State the blood parasite species.
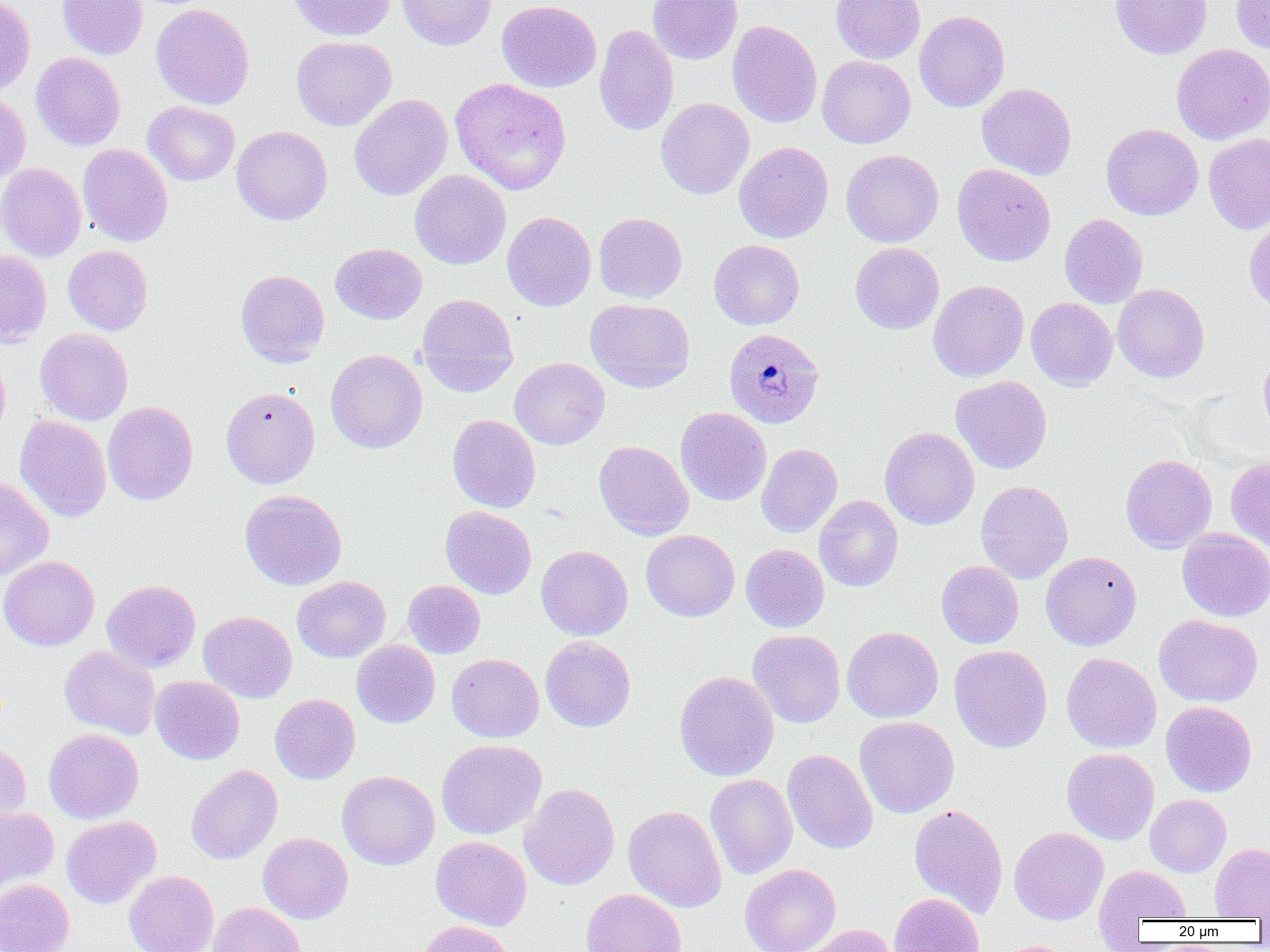
Plasmodium malariae.

image size = 1270×952 pixels
Plasmodium malariae-infected red blood cell locations = approximate bounding boxes as (x1,y1)-(x2,y2) corner pairs in pixels: (723,328)-(824,428)
uninfected red blood cell locations = approximate bounding boxes as (x1,y1)-(x2,y2) corner pairs in pixels: (0,0)-(35,98), (57,0)-(148,60), (287,0)-(395,41), (396,0)-(497,50), (497,0)-(601,92), (648,0)-(743,64), (831,0)-(925,63), (1110,0)-(1213,59), (1231,0)-(1270,54), (151,3)-(254,109), (914,11)-(1010,112), (727,20)-(822,128), (594,24)-(679,136), (291,36)-(397,131), (1171,44)-(1270,144), (30,52)-(125,151), (817,56)-(915,148), (450,77)-(571,195), (976,83)-(1077,180), (0,93)-(31,183), (349,94)-(453,201), (656,98)-(755,199), (143,101)-(240,186), (1101,124)-(1203,220), (231,126)-(332,225), (1203,132)-(1270,234), (734,141)-(833,243), (77,144)-(172,247), (841,149)-(944,247), (0,163)-(86,261), (951,163)-(1056,266), (410,170)-(511,269), (502,211)-(596,311), (594,212)-(687,303), (1059,214)-(1148,308), (1243,215)-(1270,314), (709,240)-(805,330), (850,242)-(944,334), (330,243)-(427,324), (62,245)-(153,335), (0,250)-(52,346), (235,269)-(329,367), (928,280)-(1029,382), (1112,284)-(1209,382), (416,293)-(519,396), (1026,297)-(1118,390), (585,299)-(695,393), (35,328)-(133,425), (325,349)-(427,453), (0,350)-(11,443), (1258,352)-(1270,437), (509,357)-(610,449), (951,375)-(1052,474), (221,386)-(320,488), (102,401)-(198,505), (675,407)-(771,506), (447,414)-(540,513), (14,415)-(111,522), (879,426)-(979,529), (594,441)-(694,540), (756,443)-(843,537), (1120,454)-(1216,553), (1225,457)-(1270,552), (0,476)-(54,581), (975,481)-(1073,583), (240,490)-(346,590), (814,495)-(903,592), (440,506)-(536,598), (1177,528)-(1270,622), (641,530)-(739,621), (741,544)-(829,632), (536,545)-(632,640), (1041,551)-(1142,650), (0,555)-(100,651), (936,560)-(1024,648), (292,576)-(390,662), (101,580)-(200,672), (403,580)-(485,658), (198,611)-(297,703), (1154,614)-(1263,707), (842,627)-(943,722), (748,630)-(845,727), (540,636)-(636,732), (352,640)-(440,728), (60,645)-(159,740), (949,645)-(1052,753), (1061,652)-(1161,753), (447,654)-(544,742), (675,670)-(779,781), (150,676)-(245,765), (270,694)-(360,785), (1160,701)-(1257,796), (854,716)-(959,818), (43,728)-(144,823), (436,740)-(547,839), (0,741)-(31,830), (1061,748)-(1159,845), (783,749)-(878,854), (186,764)-(283,864), (337,770)-(439,870), (705,774)-(798,879), (519,783)-(620,890), (1145,794)-(1231,877), (908,804)-(1008,918), (623,805)-(727,912), (0,807)-(59,897), (61,816)-(161,908), (1009,826)-(1109,925), (258,833)-(353,924), (431,836)-(531,931), (1209,843)-(1270,919), (740,863)-(841,952), (1095,866)-(1191,924), (124,870)-(218,952), (0,880)-(74,952), (581,889)-(687,952), (888,892)-(984,952), (208,902)-(306,952), (415,920)-(515,952), (800,924)-(896,952), (990,940)-(1080,952)
preparation = thin blood smear
field of view = one of a larger specimen
magnification = 1000x
modality = light microscopy